Outline each blood parasite and name the species.
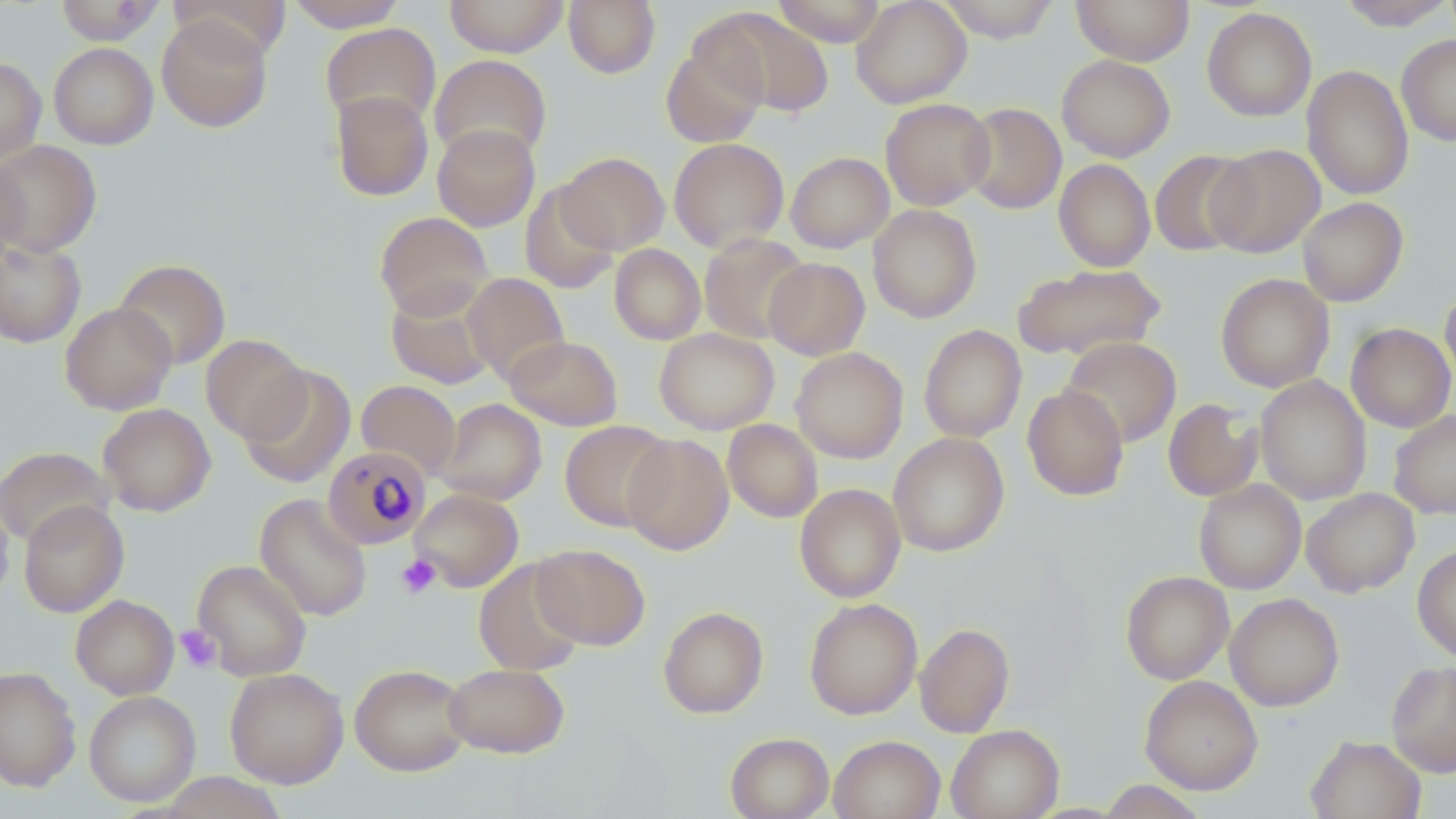
Approximate bounding boxes as named x1/y1/x2/y2 corners in pixels.
Plasmodium malariae-infected red blood cells: (x1=323, y1=446, x2=431, y2=550).
No Plasmodium falciparum, Plasmodium ovale, Plasmodium vivax, Babesia divergens, or Trypanosoma brucei observed.

slide-level diagnosis = Plasmodium malariae
magnification = 1000x
image size = 1456×819 pixels
stain = May-Grünwald-Giemsa
field of view = one of a larger specimen
preparation = thin blood smear
modality = optical microscopy
platelet locations = approximate bounding boxes as named x1/y1/x2/y2 corners in pixels: (x1=396, y1=554, x2=442, y2=599), (x1=175, y1=625, x2=221, y2=672)
uninfected red blood cell locations = approximate bounding boxes as named x1/y1/x2/y2 corners in pixels: (x1=54, y1=0, x2=164, y2=45), (x1=168, y1=0, x2=291, y2=60), (x1=286, y1=0, x2=406, y2=32), (x1=444, y1=0, x2=570, y2=57), (x1=563, y1=0, x2=660, y2=78), (x1=771, y1=0, x2=887, y2=46), (x1=851, y1=0, x2=972, y2=108), (x1=937, y1=0, x2=1060, y2=42), (x1=1071, y1=0, x2=1195, y2=65), (x1=1336, y1=0, x2=1456, y2=30), (x1=1202, y1=7, x2=1317, y2=122), (x1=702, y1=9, x2=832, y2=118), (x1=156, y1=14, x2=273, y2=132), (x1=320, y1=22, x2=441, y2=130), (x1=1397, y1=34, x2=1456, y2=146), (x1=660, y1=42, x2=767, y2=148), (x1=49, y1=43, x2=158, y2=149), (x1=429, y1=54, x2=552, y2=163), (x1=1057, y1=54, x2=1175, y2=162), (x1=0, y1=57, x2=46, y2=164), (x1=1302, y1=65, x2=1414, y2=200), (x1=331, y1=90, x2=434, y2=201), (x1=880, y1=98, x2=995, y2=210), (x1=961, y1=103, x2=1067, y2=214), (x1=432, y1=123, x2=540, y2=231), (x1=669, y1=137, x2=789, y2=252), (x1=0, y1=139, x2=102, y2=256), (x1=1207, y1=144, x2=1325, y2=257), (x1=1149, y1=150, x2=1255, y2=256), (x1=558, y1=151, x2=669, y2=254), (x1=786, y1=151, x2=894, y2=252), (x1=0, y1=155, x2=29, y2=266), (x1=1054, y1=158, x2=1155, y2=272), (x1=520, y1=182, x2=620, y2=294), (x1=1297, y1=197, x2=1408, y2=307), (x1=867, y1=205, x2=982, y2=323), (x1=375, y1=212, x2=493, y2=320), (x1=698, y1=233, x2=811, y2=345), (x1=0, y1=237, x2=86, y2=348), (x1=609, y1=244, x2=706, y2=345), (x1=763, y1=257, x2=870, y2=360), (x1=114, y1=258, x2=231, y2=369), (x1=1013, y1=263, x2=1165, y2=361), (x1=462, y1=272, x2=569, y2=385), (x1=1215, y1=273, x2=1335, y2=392), (x1=1440, y1=282, x2=1456, y2=389), (x1=386, y1=285, x2=496, y2=389), (x1=60, y1=302, x2=177, y2=415), (x1=1346, y1=323, x2=1456, y2=432), (x1=919, y1=324, x2=1027, y2=442), (x1=654, y1=328, x2=779, y2=434), (x1=200, y1=333, x2=309, y2=443), (x1=504, y1=335, x2=623, y2=431), (x1=1061, y1=337, x2=1182, y2=446), (x1=791, y1=347, x2=908, y2=463), (x1=240, y1=364, x2=356, y2=489), (x1=1255, y1=375, x2=1371, y2=504), (x1=356, y1=380, x2=461, y2=479), (x1=1022, y1=385, x2=1129, y2=500), (x1=437, y1=398, x2=546, y2=505), (x1=1163, y1=398, x2=1263, y2=501), (x1=98, y1=403, x2=215, y2=516), (x1=1388, y1=410, x2=1456, y2=519), (x1=723, y1=419, x2=822, y2=522), (x1=559, y1=420, x2=673, y2=531), (x1=888, y1=432, x2=1009, y2=557), (x1=622, y1=433, x2=734, y2=555), (x1=0, y1=446, x2=113, y2=548), (x1=1194, y1=480, x2=1306, y2=594), (x1=794, y1=483, x2=905, y2=602), (x1=409, y1=488, x2=523, y2=591), (x1=1301, y1=488, x2=1419, y2=597), (x1=0, y1=489, x2=14, y2=607), (x1=254, y1=493, x2=372, y2=621), (x1=18, y1=500, x2=129, y2=617), (x1=531, y1=543, x2=650, y2=650), (x1=1413, y1=544, x2=1456, y2=662), (x1=192, y1=559, x2=311, y2=681), (x1=473, y1=559, x2=586, y2=676), (x1=1121, y1=571, x2=1234, y2=684), (x1=1225, y1=593, x2=1344, y2=711), (x1=71, y1=595, x2=179, y2=699), (x1=804, y1=597, x2=923, y2=720), (x1=657, y1=606, x2=769, y2=718), (x1=915, y1=623, x2=1014, y2=738), (x1=1386, y1=660, x2=1456, y2=777), (x1=443, y1=663, x2=569, y2=759), (x1=349, y1=664, x2=472, y2=775), (x1=0, y1=666, x2=81, y2=792), (x1=225, y1=668, x2=348, y2=788), (x1=1140, y1=675, x2=1263, y2=795), (x1=84, y1=690, x2=201, y2=806), (x1=947, y1=724, x2=1064, y2=819), (x1=725, y1=732, x2=834, y2=819), (x1=828, y1=735, x2=944, y2=819), (x1=1306, y1=735, x2=1426, y2=819), (x1=158, y1=772, x2=287, y2=818), (x1=1097, y1=780, x2=1208, y2=818)